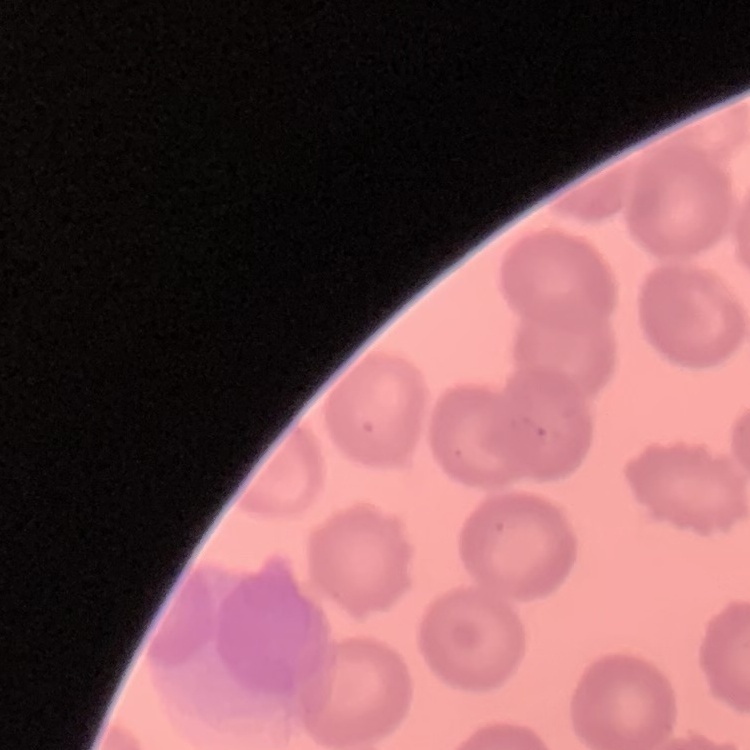

Summary:
  - Erythrocyte morphology: no rouleaux formation
  - Preparation: thin blood film
  - Image type: square crop of a larger photomicrograph
  - Stain: Field's or Giemsa